Identify the parasite.
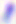

This is Toxoplasma gondii.

Captured at 400x magnification. Micrograph.